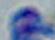
Photomicrograph. Captured at 1000x magnification. Toxoplasma gondii is seen.